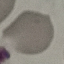

Result: no malaria parasites seen. Photographed with a smartphone camera at the microscope eyepiece. Thin blood smear. Giemsa stain. Cell patch, automatically extracted from a larger field of view and resized to 64 × 64 pixels.